Describe the morphology of the red blood cells.
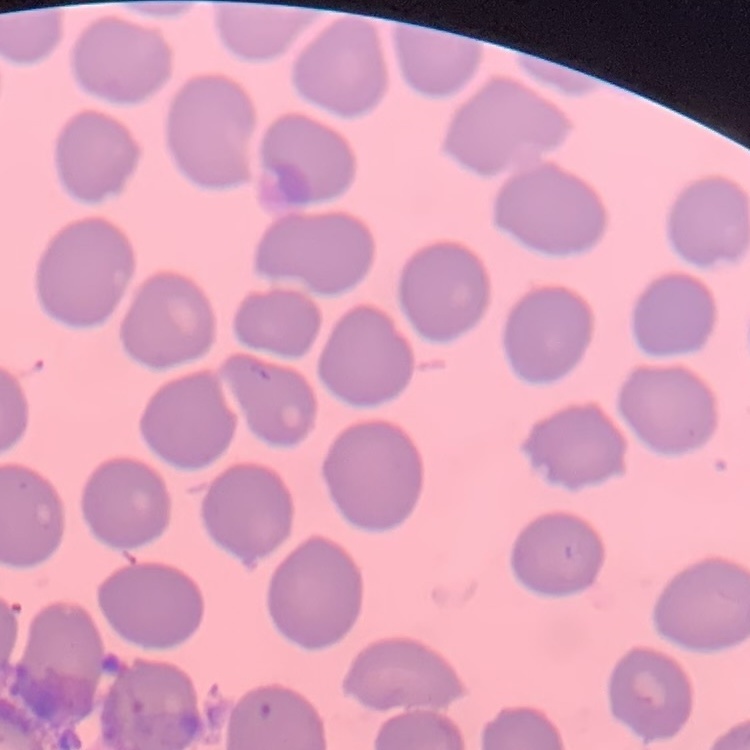

No rouleaux formation.

Thin blood smear. Stained with either Field's or Giemsa. One tile cut from a larger photomicrograph.